Report the malaria status of this cell.
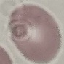
Uninfected.

Summary:
  - Stain: Giemsa
  - Capture: smartphone camera at the microscope eyepiece
  - Image type: automatically extracted cell patch, resized to 64 × 64 pixels
  - Preparation: thin smear